State the preparation type.
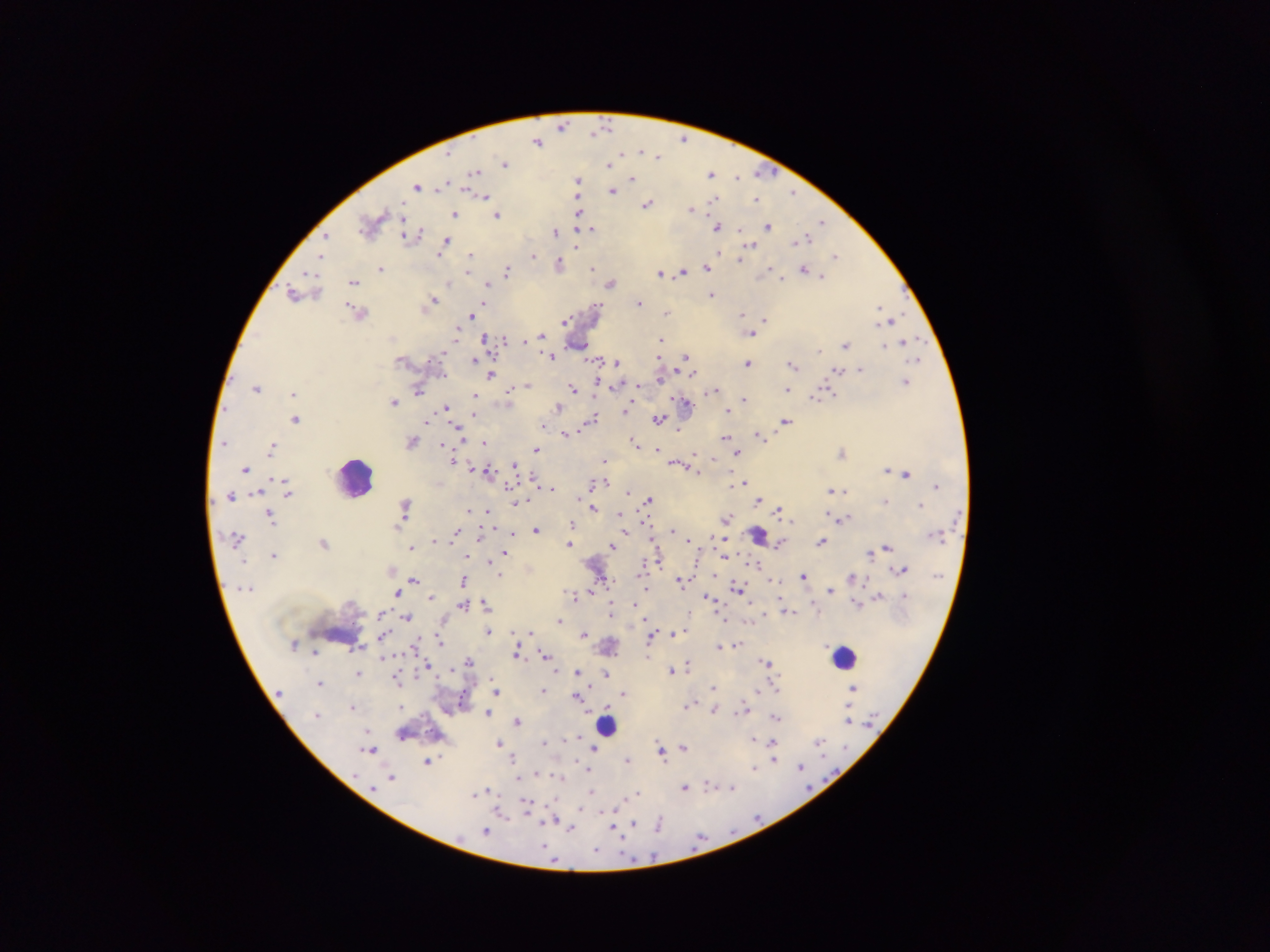
Thick blood film.

field_of_view: single
country: Ghana
malaria_parasite_locations: 'approximate centers as [x, y] in pixels: [561, 127], [607, 127], [589, 129], [683, 137], [538, 140], [640, 148], [655, 154], [504, 162], [608, 164], [474, 170], [711, 172], [758, 173], [578, 178], [737, 178], [631, 179], [443, 184], [416, 185], [438, 188], [794, 190], [613, 191], [484, 196], [757, 199], [712, 203], [647, 204], [691, 210], [455, 214], [499, 214], [576, 217], [823, 222], [718, 226], [590, 227], [768, 227], [738, 229], [556, 231], [419, 234], [327, 235], [405, 236], [447, 240], [794, 242], [753, 243], [718, 251], [471, 255], [440, 256], [533, 257], [322, 258], [741, 258], [835, 258], [559, 261], [706, 266], [381, 268], [593, 268], [804, 268], [506, 270], [468, 272], [682, 272], [309, 273], [661, 274], [781, 278], [353, 281], [488, 282], [611, 284], [293, 291], [711, 295], [433, 299], [598, 302], [639, 303], [350, 304], [484, 305], [879, 306], [667, 311], [741, 313], [472, 314], [894, 318], [765, 319], [566, 320], [456, 334], [661, 334], [543, 335], [751, 336], [485, 338], [661, 339], [505, 341], [525, 342], [846, 343], [883, 344], [820, 351], [687, 356], [551, 357], [477, 359], [586, 359], [917, 359], [657, 360], [429, 361], [616, 361], [749, 364], [794, 365], [861, 367], [838, 370], [858, 370], [679, 372], [490, 375], [695, 375], [444, 376], [658, 378], [597, 380], [906, 382], [527, 384], [257, 387], [638, 387], [573, 388], [788, 389], [713, 390], [293, 392], [418, 392], [508, 392], [575, 392], [791, 392], [834, 393], [474, 394], [815, 399], [394, 401], [743, 401], [631, 402], [686, 402], [446, 406], [558, 406], [626, 408], [726, 410], [473, 415], [595, 416], [294, 418], [472, 419], [658, 419], [785, 420], [426, 422], [588, 422], [544, 423], [678, 430], [563, 433], [758, 434], [724, 438], [635, 440], [728, 441], [226, 442], [484, 443], [443, 444], [273, 445], [656, 447], [536, 449], [738, 452], [844, 453], [697, 454], [606, 461], [454, 462], [512, 464], [677, 464], [491, 466], [245, 469], [885, 469], [890, 471], [907, 473], [605, 481], [744, 481], [590, 484], [510, 485], [936, 485], [548, 488], [833, 490], [842, 492], [629, 493], [230, 495], [288, 495], [649, 499], [759, 501], [886, 501], [515, 502], [407, 504], [921, 505], [593, 507], [470, 509], [487, 510], [779, 511], [619, 512], [271, 515], [488, 517], [574, 519], [846, 519], [727, 520], [792, 521], [956, 521], [272, 523], [573, 524], [535, 529], [672, 531], [455, 532], [625, 532], [942, 532], [511, 533], [479, 535], [929, 535], [712, 536], [452, 537], [652, 539], [686, 539], [432, 540], [618, 542], [821, 542], [568, 544], [411, 545], [612, 546], [886, 546], [507, 548], [504, 552], [868, 553], [273, 555], [467, 558], [486, 560], [647, 562], [698, 562], [755, 565], [901, 568], [501, 574], [715, 576], [803, 576], [604, 577], [413, 578], [852, 578], [463, 579], [776, 580], [680, 581], [593, 586], [738, 589], [647, 590], [830, 590], [875, 590], [398, 593], [879, 594], [574, 595], [431, 597], [708, 597], [485, 602], [462, 605], [635, 605], [612, 610], [793, 612], [766, 613], [380, 614], [686, 615], [405, 616], [724, 619], [559, 621], [489, 631], [529, 631], [513, 632], [584, 633], [652, 633], [674, 634], [440, 640], [738, 645], [718, 646], [413, 647], [720, 647], [517, 653], [545, 654], [383, 656], [469, 660], [764, 661], [686, 663], [428, 666], [577, 671], [672, 671], [606, 672], [393, 676], [318, 684], [852, 686], [588, 687], [713, 687], [775, 687], [496, 690], [544, 691], [623, 693], [575, 694], [755, 694], [495, 695], [460, 699], [690, 701], [399, 705], [351, 706], [605, 706], [687, 706], [739, 710], [487, 711], [713, 711], [776, 717], [846, 718], [517, 721], [752, 739], [819, 741], [544, 742], [498, 743], [773, 743], [660, 746], [684, 746], [371, 748], [365, 750], [594, 750], [661, 752], [513, 758], [627, 758], [664, 759], [775, 760], [426, 763], [800, 765], [754, 768], [587, 770], [535, 773], [393, 780], [709, 785], [488, 788], [686, 788], [733, 788], [588, 790], [637, 791], [472, 795], [524, 803], [617, 806], [580, 809], [757, 815], [504, 816], [662, 819], [557, 820], [634, 822], [546, 824], [660, 824], [570, 828], [614, 829], [486, 831], [544, 848], [596, 851]'
capture: mobile-phone photograph through a microscope
image_size: 1270×952 pixels
leukocyte_locations: 'approximate centers as [x, y] in pixels: [352, 480], [844, 655], [608, 723]'